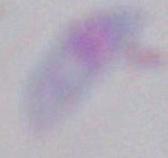
Summary:
  - Identification: Toxoplasma gondii
  - Modality: photomicrograph
  - Magnification: 1000x